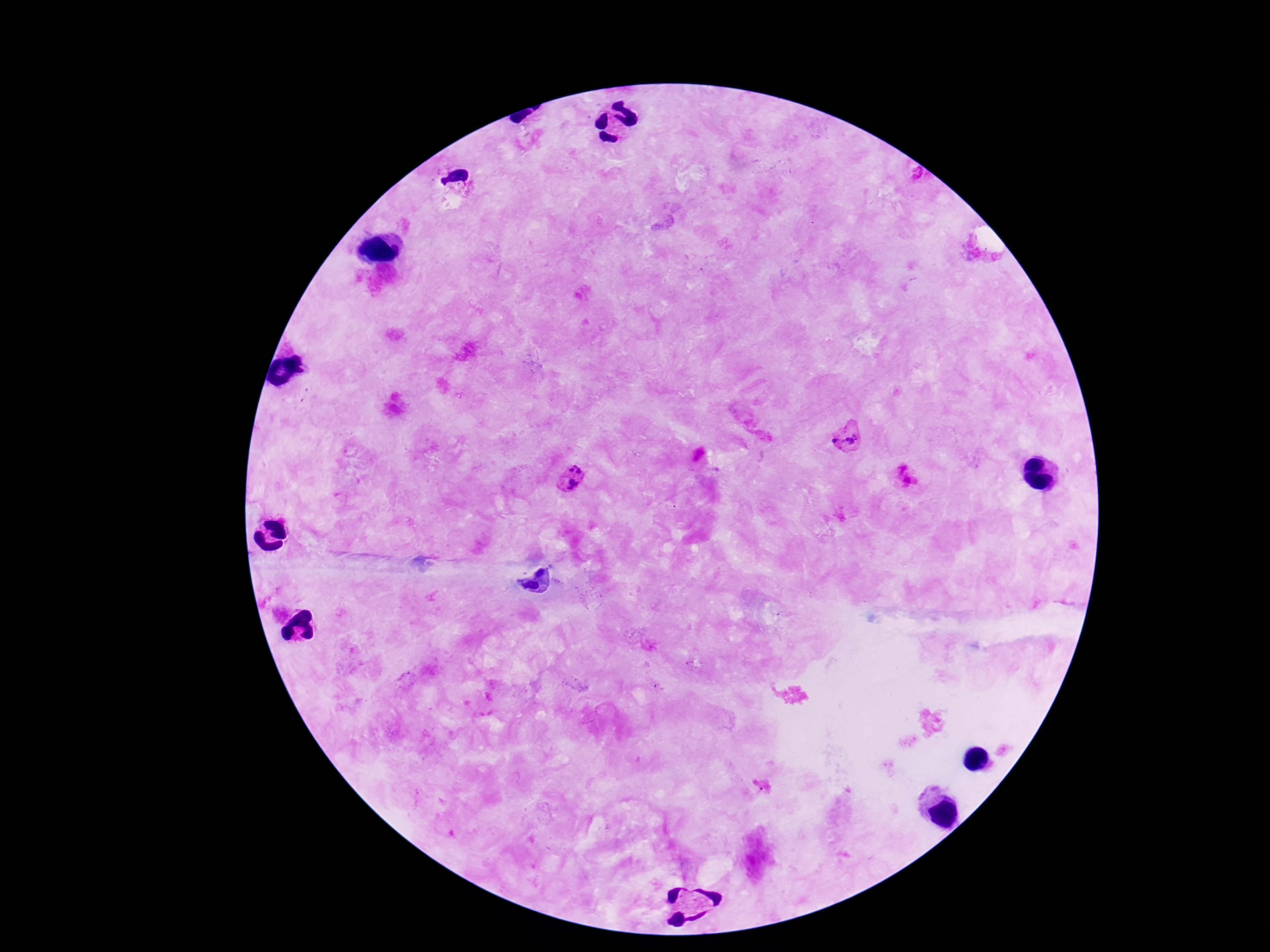

{
  "magnification": "100x",
  "patient_malaria_status": "positive",
  "field_of_view": "single",
  "plasmodium_parasite_locations": "approximate object centers, in pixels from the top-left corner: (x=847, y=439), (x=572, y=478)",
  "preparation": "thick blood smear",
  "capture": "smartphone camera through the microscope eyepiece",
  "image_size": "1270×952 pixels",
  "stain": "Giemsa"
}